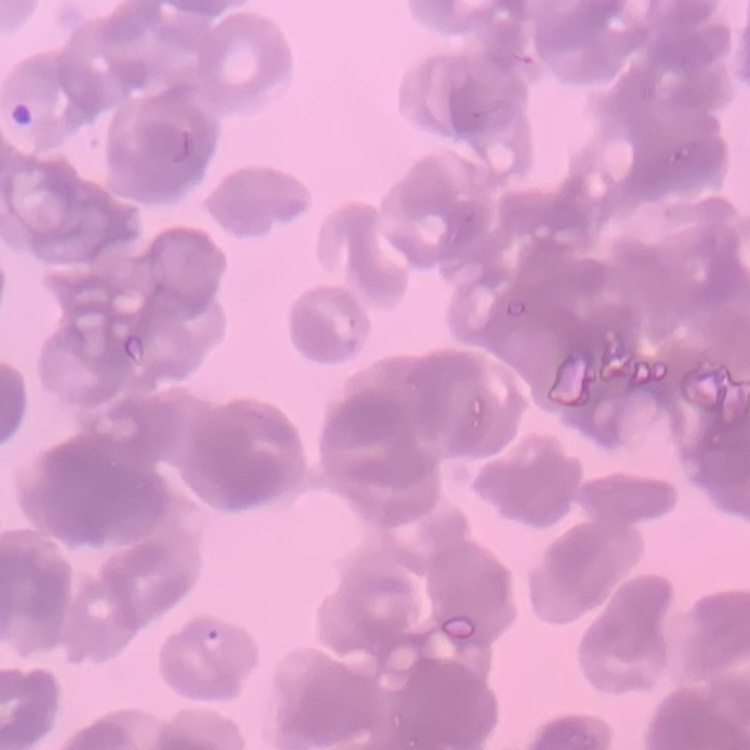

Summary:
  - Erythrocyte morphology: rouleaux formation
  - Stain: Field's or Giemsa
  - Preparation: thin blood film
  - Image type: square crop of a larger photomicrograph